Locate every uninfected red blood cell.
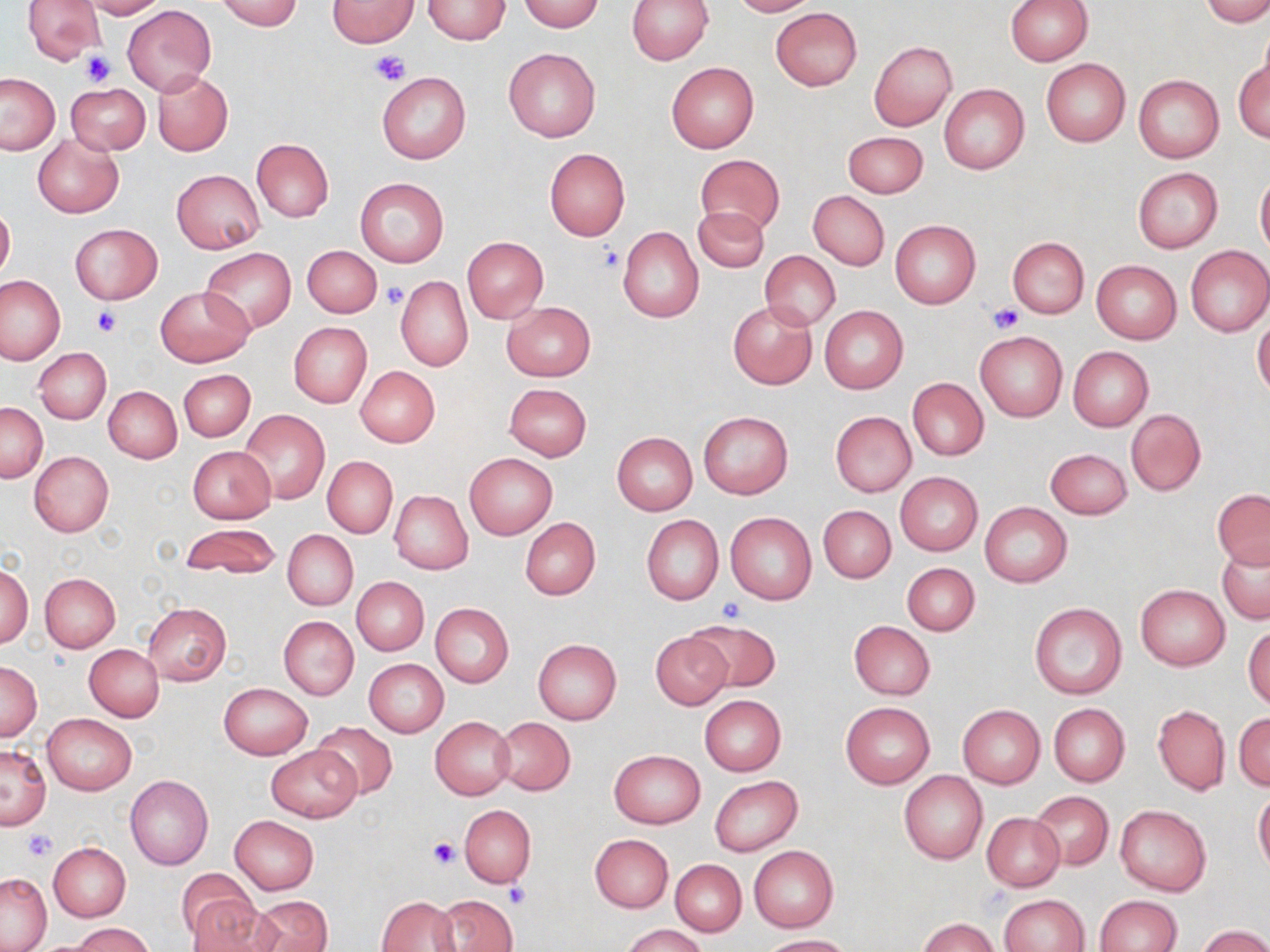

Approximate bounding boxes as [x1, y1, x2, y2] in pixels.
Uninfected red blood cells: [21, 0, 105, 64], [79, 0, 165, 19], [217, 0, 304, 30], [326, 0, 421, 47], [422, 0, 511, 44], [627, 0, 711, 64], [728, 0, 815, 16], [1006, 0, 1092, 65], [1202, 0, 1270, 27], [515, 1, 604, 31], [122, 5, 216, 96], [769, 8, 862, 91], [867, 40, 956, 131], [503, 48, 600, 141], [1235, 56, 1269, 145], [1040, 58, 1131, 147], [666, 61, 759, 153], [152, 71, 232, 156], [376, 72, 470, 164], [0, 74, 59, 154], [1133, 74, 1224, 163], [65, 83, 150, 154], [939, 84, 1029, 175], [843, 131, 928, 199], [33, 133, 125, 218], [252, 138, 333, 222], [544, 148, 630, 240], [695, 153, 784, 236], [1132, 167, 1222, 253], [171, 170, 264, 253], [1256, 171, 1270, 257], [354, 177, 448, 268], [808, 190, 889, 270], [0, 204, 15, 280], [693, 206, 769, 273], [889, 220, 981, 310], [69, 224, 161, 304], [617, 227, 704, 324], [461, 236, 548, 324], [1007, 236, 1090, 318], [1186, 245, 1270, 337], [303, 246, 382, 317], [201, 248, 296, 333], [759, 250, 841, 331], [1091, 260, 1182, 345], [0, 275, 67, 366], [395, 275, 474, 372], [156, 285, 253, 367], [727, 301, 817, 389], [501, 302, 595, 381], [819, 306, 908, 394], [1253, 315, 1270, 399], [289, 322, 372, 408], [975, 331, 1066, 421], [1068, 346, 1153, 432], [34, 347, 112, 423], [355, 366, 440, 448], [179, 369, 255, 442], [907, 377, 989, 461], [503, 383, 592, 460], [104, 386, 182, 463], [0, 402, 47, 481], [1125, 409, 1206, 496], [240, 410, 330, 504], [829, 411, 916, 497], [698, 412, 793, 500], [612, 432, 698, 515], [187, 445, 276, 523], [1045, 448, 1132, 518], [29, 451, 114, 536], [464, 453, 557, 539], [322, 456, 397, 538], [895, 472, 983, 556], [1212, 489, 1270, 569], [389, 490, 473, 575], [980, 503, 1072, 586], [818, 505, 895, 583], [725, 512, 817, 605], [641, 515, 724, 605], [519, 518, 600, 600], [179, 523, 280, 579], [284, 531, 357, 610], [1216, 539, 1269, 625], [902, 563, 980, 635], [0, 564, 33, 646], [39, 572, 120, 651], [352, 577, 429, 656], [1135, 584, 1229, 670], [143, 602, 231, 685], [431, 603, 513, 687], [1031, 603, 1126, 699], [279, 616, 358, 699], [683, 618, 780, 696], [849, 621, 934, 699], [1244, 624, 1270, 708], [650, 631, 732, 709], [532, 639, 621, 725], [85, 645, 164, 721], [364, 658, 449, 737], [0, 661, 42, 740], [219, 683, 312, 759], [705, 692, 792, 856], [699, 694, 786, 775], [841, 702, 934, 788], [958, 704, 1045, 788], [1049, 704, 1130, 786], [1153, 704, 1230, 796], [42, 712, 138, 794], [1234, 712, 1270, 791], [431, 716, 514, 800], [493, 718, 575, 795], [310, 721, 399, 799], [0, 743, 51, 829], [265, 745, 360, 822], [609, 749, 705, 828], [898, 771, 988, 864], [126, 775, 213, 869], [710, 776, 803, 856], [1254, 790, 1270, 874], [1032, 791, 1113, 869], [1115, 804, 1211, 897], [459, 805, 536, 888], [981, 812, 1065, 891], [230, 815, 319, 894], [591, 834, 673, 913], [48, 842, 131, 921], [749, 846, 838, 931], [671, 859, 746, 936], [175, 867, 260, 945], [0, 872, 52, 951], [999, 894, 1089, 952], [187, 895, 278, 952], [246, 895, 333, 952], [436, 895, 516, 952], [1094, 895, 1181, 952], [377, 896, 459, 952], [918, 917, 997, 952], [72, 923, 153, 952], [622, 925, 707, 952], [1198, 925, 1270, 952], [759, 934, 852, 951].

slide-level diagnosis = negative for blood parasites
stain = May-Grünwald-Giemsa
modality = optical microscopy
image size = 1270×952 pixels
field of view = single
platelet locations = approximate bounding boxes as [x1, y1, x2, y2] in pixels: [370, 48, 412, 86], [80, 49, 116, 85], [594, 243, 626, 273], [380, 282, 407, 309], [988, 302, 1023, 334], [92, 306, 121, 336], [718, 598, 750, 623], [25, 829, 56, 860], [428, 837, 459, 868], [505, 883, 530, 906]
preparation = thin blood smear
magnification = 1000x